State which cell type is depicted.
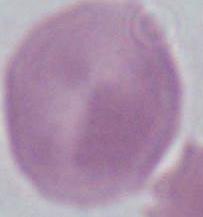
An erythrocyte.

Micrograph. Captured at 1000x magnification.